Classify this cell by malaria status.
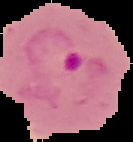

Parasitized.

Summary:
  - Preparation: thin blood smear
  - Image type: cell region segmented out of the field of view; surrounding area masked to black
  - Image size: 133×142 pixels